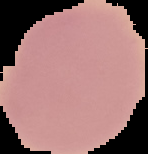 From a thin blood smear. Malaria status: uninfected. Segmented cell region on a black background. Image is 148×154 pixels.